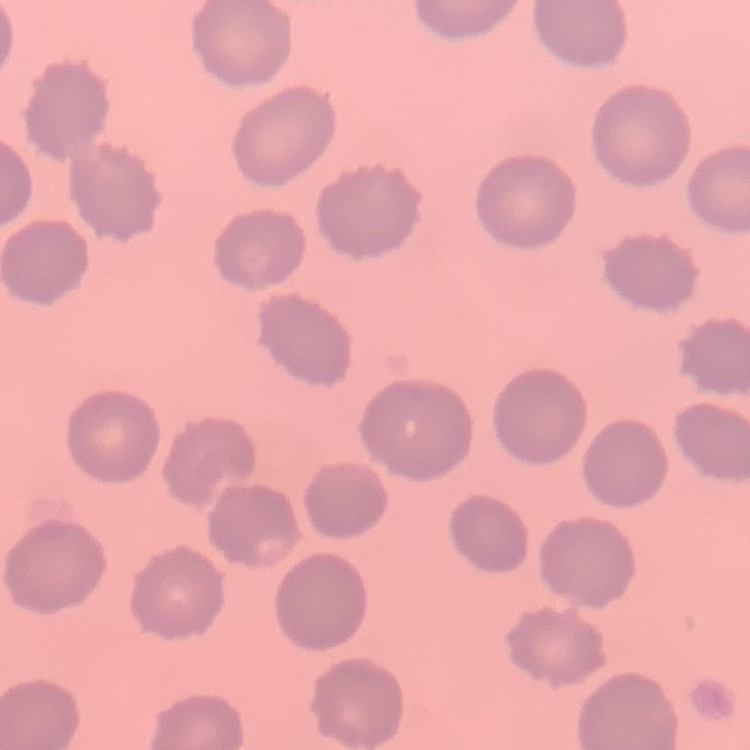
{
  "erythrocyte_morphology": "no rouleaux formation",
  "preparation": "thin blood smear",
  "image_type": "one tile cut from a larger photomicrograph",
  "stain": "Field's or Giemsa"
}